Locate and identify every blood parasite.
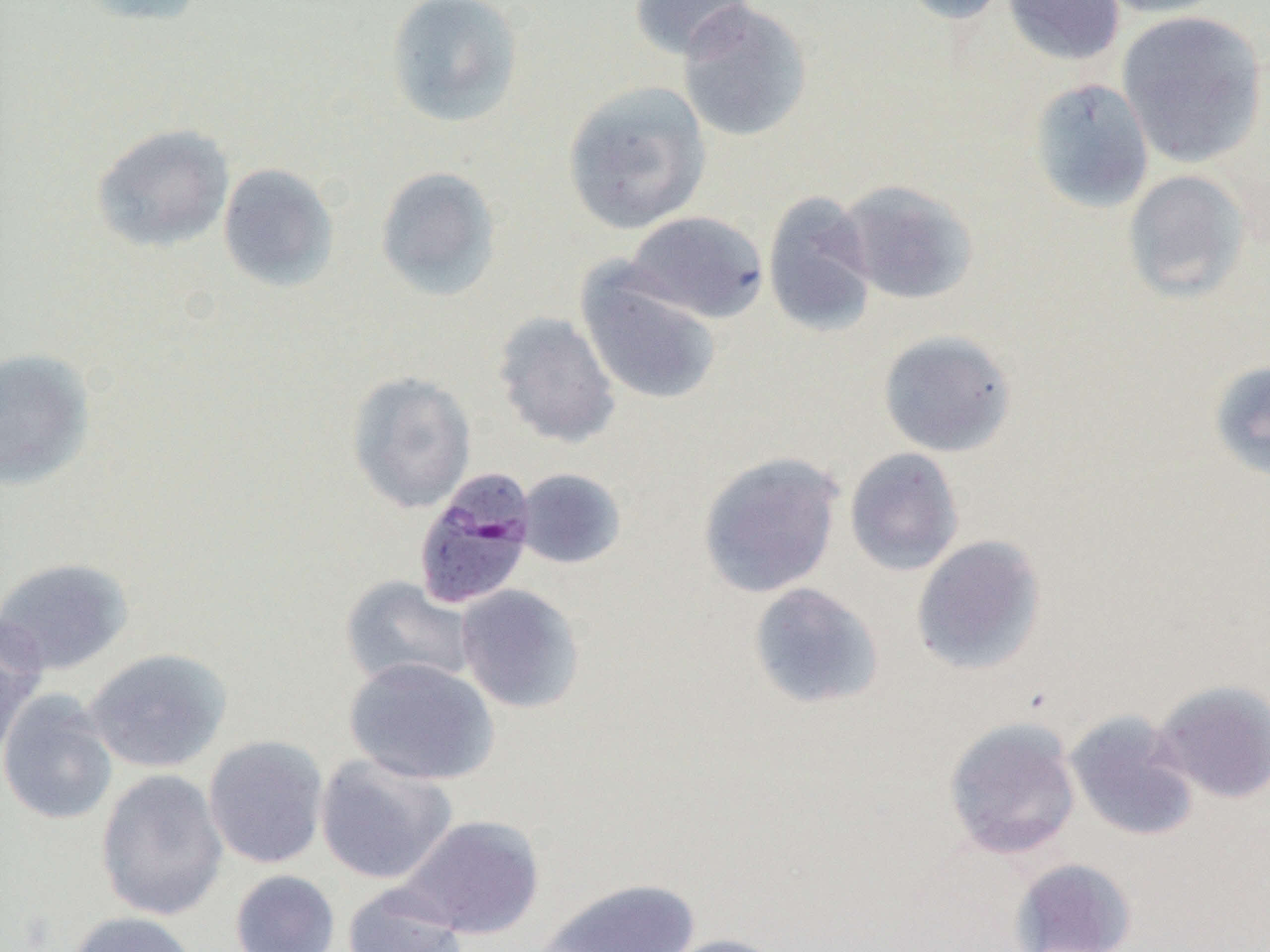

Approximate bounding boxes as (x1,y1)-(x2,y2) corner pairs in pixels.
Plasmodium malariae-infected red blood cells: (412,468)-(537,611).
No Plasmodium falciparum, Plasmodium ovale, Plasmodium vivax, Babesia divergens, or Trypanosoma brucei observed.

Summary:
  - Uninfected red blood cell locations: (75,0)-(205,27), (384,0)-(525,129), (629,0)-(757,61), (897,0)-(1013,25), (1001,0)-(1125,66), (1093,0)-(1230,19), (676,1)-(813,143), (1116,10)-(1267,168), (1027,77)-(1154,214), (562,81)-(712,235), (91,123)-(235,253), (217,163)-(339,292), (375,166)-(502,301), (1122,169)-(1250,303), (836,179)-(978,305), (762,191)-(879,338), (624,211)-(769,324), (575,266)-(722,406), (492,311)-(621,449), (876,329)-(1017,458), (0,348)-(96,490), (1207,359)-(1270,481), (346,370)-(476,514), (844,447)-(964,577), (697,451)-(844,598), (514,468)-(627,569), (911,534)-(1047,676), (0,557)-(135,676), (339,575)-(477,691), (747,581)-(884,710), (455,584)-(586,714), (0,612)-(46,759), (84,648)-(231,773), (343,657)-(499,785), (1152,679)-(1270,804), (0,691)-(119,825), (1064,710)-(1200,842), (943,716)-(1082,860), (203,735)-(329,869), (314,754)-(458,884), (95,768)-(228,921), (399,814)-(545,939), (1009,857)-(1137,952), (230,869)-(340,952), (536,878)-(700,951), (342,883)-(468,952), (65,911)-(200,952), (654,933)-(790,952)
  - Slide-level diagnosis: Plasmodium malariae
  - Preparation: thin blood film
  - Field of view: single
  - Magnification: 1000x
  - Image size: 1270×952 pixels
  - Modality: light microscopy